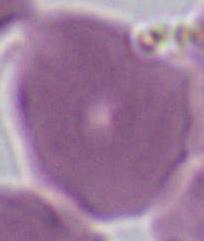
Summary:
  - Identification: red blood cell
  - Modality: micrograph
  - Magnification: 1000x